Identify the parasite.
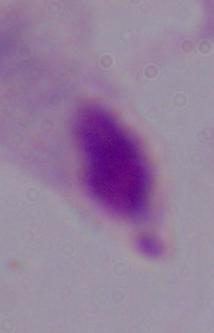
A trichomonad.

Summary:
  - Modality: micrograph
  - Magnification: 1000x